Report the malaria status of this cell.
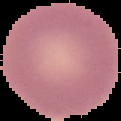

It is uninfected.

image type = segmented cell region with the area outside set to black
image size = 121×121 pixels
preparation = thin blood film